Look for Plasmodium parasites.
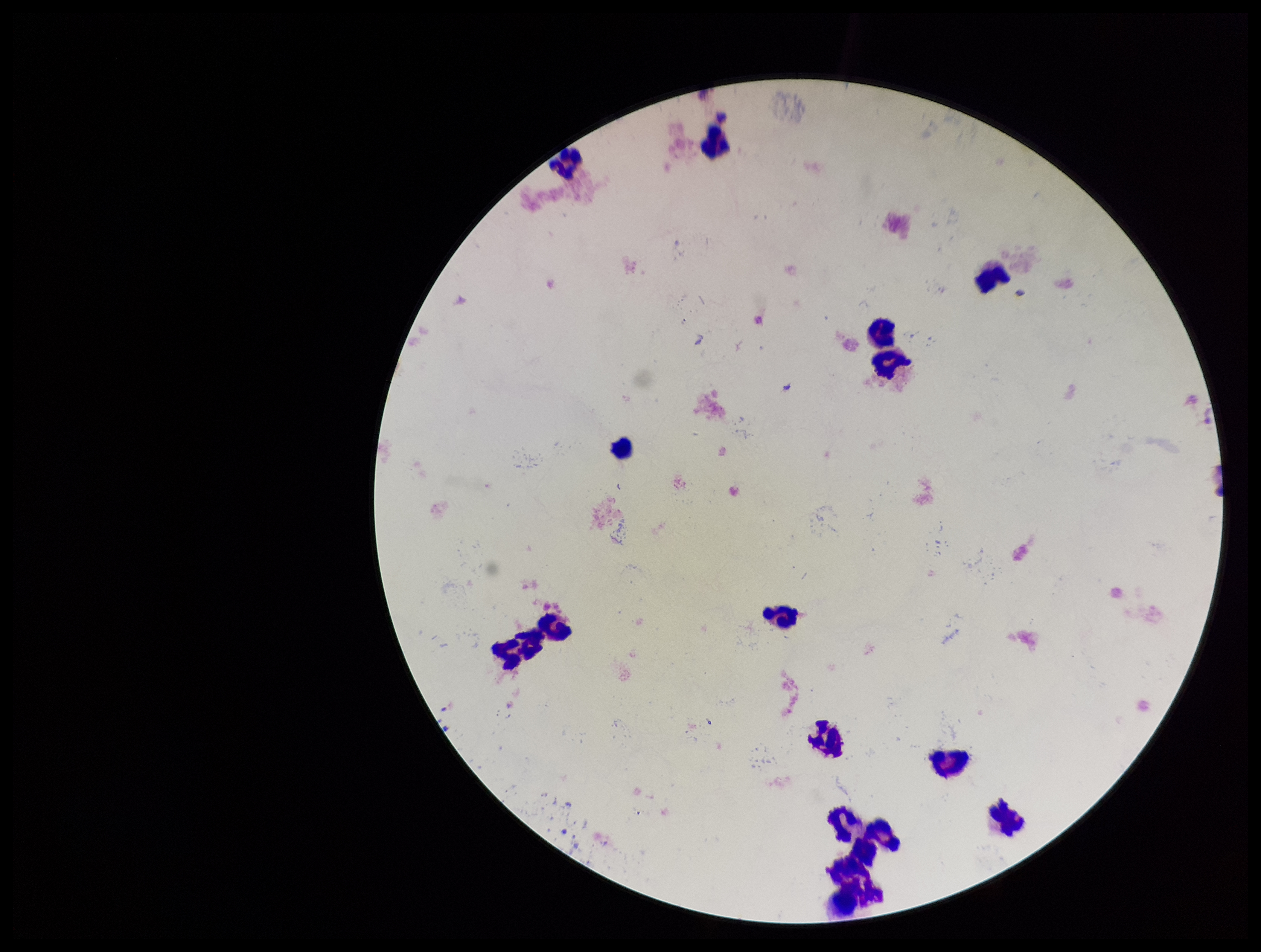
None detected.

Summary:
  - Image size: 1261×952 pixels
  - Field of view: one from this slide
  - Parasite count: 0
  - Patient malaria status: negative
  - Leukocyte count: 16
  - Preparation: thick
  - Stain: Giemsa
  - Capture: smartphone photograph through the microscope eyepiece